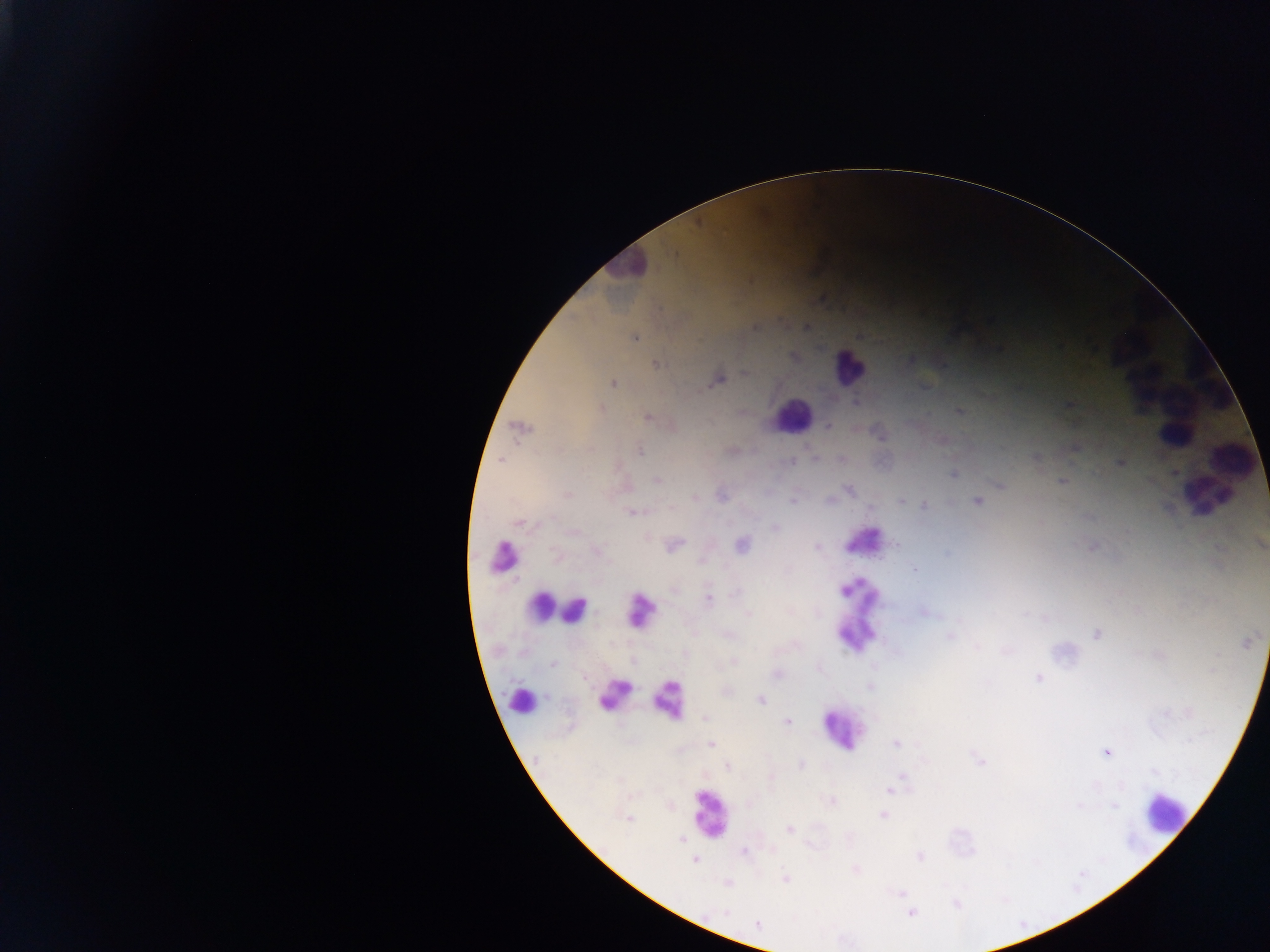

Approximate centers as {x, y} in pixels. Leukocyte locations: {624, 268}, {1119, 342}, {1197, 351}, {847, 368}, {1151, 387}, {1212, 390}, {792, 415}, {1175, 433}, {1237, 452}, {1203, 494}, {862, 542}, {502, 556}, {539, 610}, {860, 610}, {640, 611}, {574, 613}, {615, 695}, {667, 697}, {527, 701}, {840, 730}, {710, 813}, {1164, 813}. Plasmodium parasite locations: {754, 327}, {805, 327}, {634, 337}, {794, 357}, {656, 365}, {745, 373}, {717, 381}, {613, 383}, {855, 401}, {601, 408}, {959, 412}, {646, 416}, {828, 426}, {520, 428}, {639, 452}, {1036, 458}, {814, 459}, {501, 461}, {790, 461}, {1120, 462}, {953, 474}, {657, 480}, {1062, 481}, {1000, 487}, {849, 489}, {568, 494}, {721, 497}, {695, 498}, {793, 500}, {829, 500}, {901, 501}, {977, 501}, {924, 506}, {632, 513}, {520, 524}, {775, 527}, {741, 544}, {897, 544}, {1260, 544}, {675, 545}, {816, 547}, {597, 551}, {947, 554}, {914, 570}, {734, 594}, {709, 598}, {924, 612}, {748, 614}, {1044, 618}, {728, 635}, {1096, 635}, {950, 636}, {1246, 643}, {978, 647}, {1006, 652}, {734, 661}, {552, 664}, {777, 674}, {1038, 678}, {870, 686}, {761, 700}, {705, 718}, {788, 722}, {711, 744}, {896, 744}, {1106, 752}, {979, 761}, {802, 765}, {728, 767}, {902, 776}, {896, 785}, {890, 790}, {830, 801}, {1079, 806}, {1114, 806}, {884, 815}, {629, 818}, {790, 829}, {681, 840}, {744, 852}, {919, 856}, {694, 860}, {856, 869}, {785, 878}, {728, 884}, {900, 893}, {957, 904}, {724, 912}, {911, 913}, {757, 924}. Thick blood film. Mobile-phone photograph taken through the microscope. Image is 1270×952 pixels. Sample from Ghana. One field of view.